Comment on the morphology of the red blood cells.
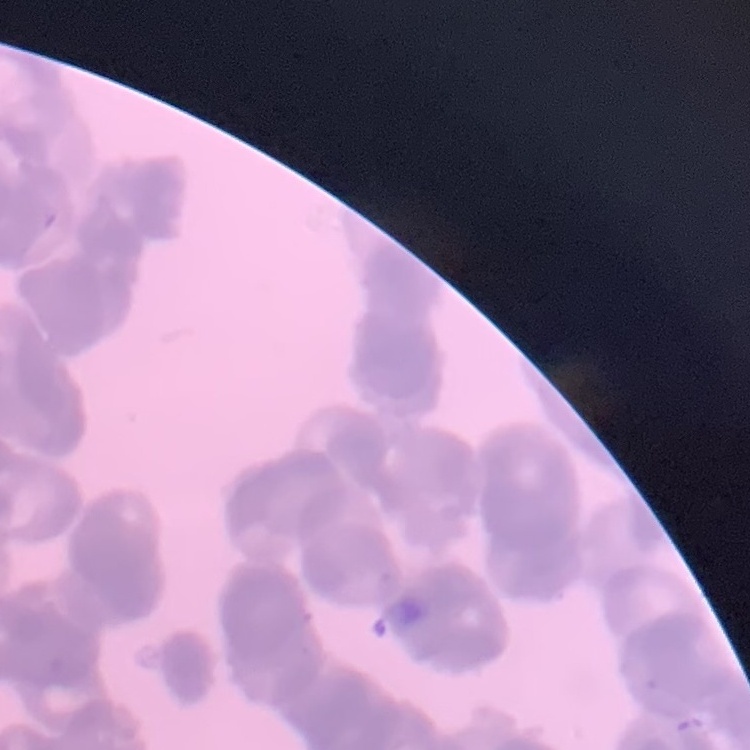

Rouleaux formation.

Thin peripheral smear. Square crop of a larger photomicrograph. Field's or Giemsa stain.